Give the preparation type.
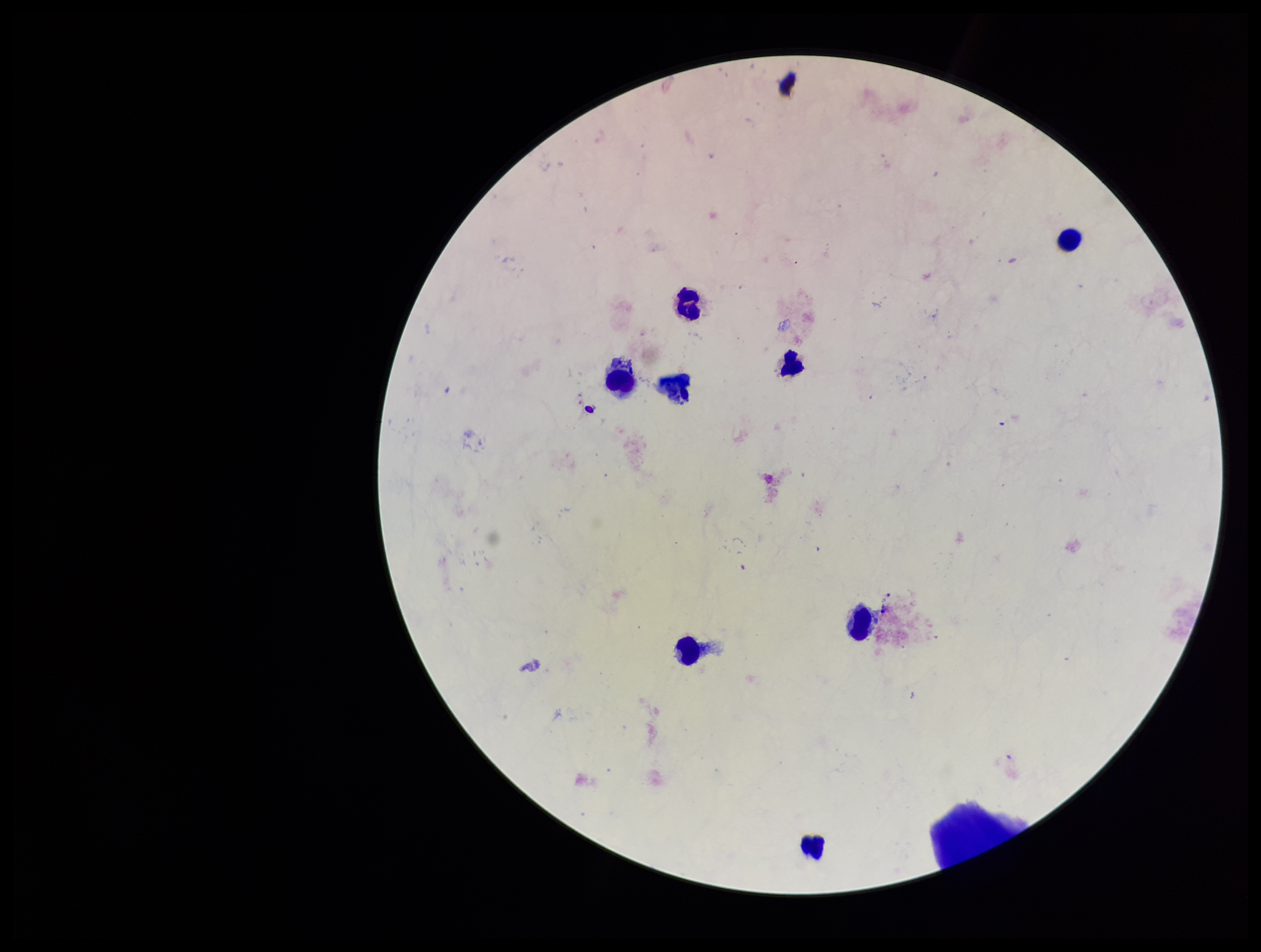

A thick smear.

Giemsa stain. Leukocyte count: 8. Patient malaria status: negative. Smartphone photograph taken through the eyepiece of a microscope. Parasite count: 0. Image is 1261×952 pixels. One field from this slide. Plasmodium parasites: none identified.